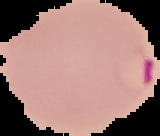

Summary:
  - Result: Plasmodium parasites identified
  - Preparation: thin blood smear
  - Image type: segmented cell region on a black background
  - Image size: 160×136 pixels